Classify this cell by malaria status.
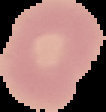

It is uninfected.

image type = segmented cell region with the area outside set to black
preparation = thin blood smear
image size = 106×112 pixels